Describe the morphology of the red blood cells.
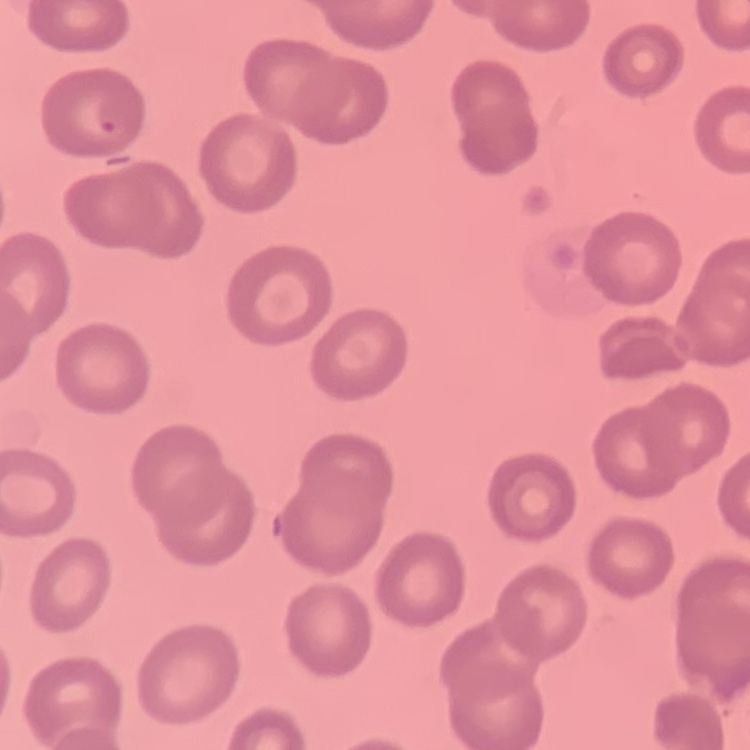

No rouleaux formation.

preparation = thin blood smear
image type = one tile cut from a larger photomicrograph
stain = Field's or Giemsa